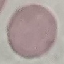
{
  "result": "no malaria parasites seen",
  "preparation": "thin blood film",
  "image_type": "cell patch, automatically extracted from a larger field of view and resized to 64 × 64 pixels",
  "stain": "Giemsa",
  "capture": "smartphone through the microscope eyepiece"
}